Classify this cell by malaria status.
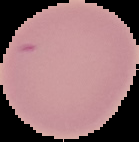

Uninfected.

From a thin blood film. The area outside the segmented cell region is set to black. Image is 139×142 pixels.